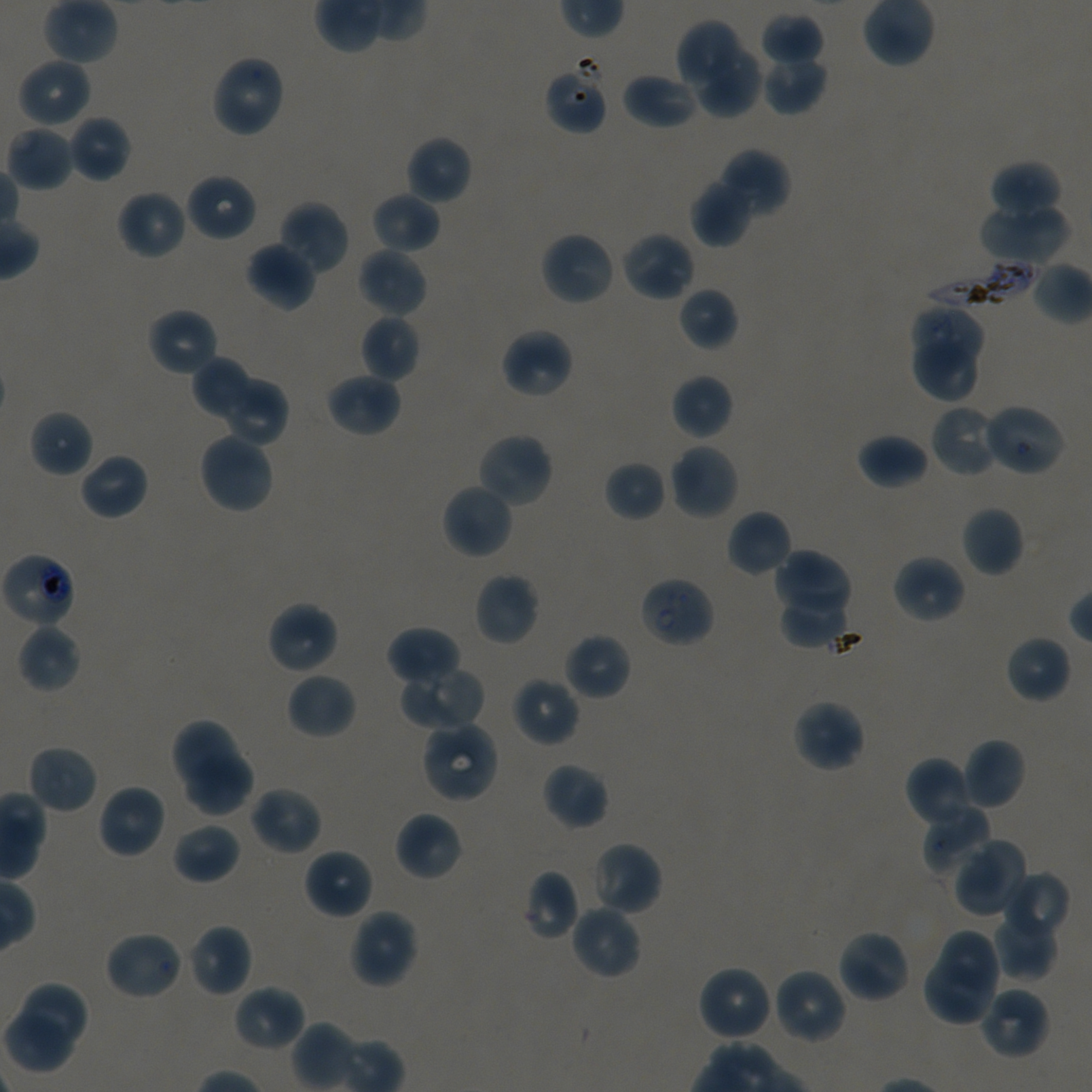

Approximate bounding rectangles given as corner coordinates in pixels from the top-left. Not every red blood cell is marked. A life-cycle stage — or a range of stages, where the recorded stages span more than one — follows each staged infected red blood cell.
Summary:
  - Locations of red blood cells of indeterminate infection status: (x1=545, y1=63, x2=608, y2=135)
  - Locations of infected red blood cells: (x1=924, y1=259, x2=1039, y2=310); (x1=0, y1=551, x2=76, y2=630) trophozoite; (x1=638, y1=575, x2=716, y2=649) early ring
  - Locations of uninfected red blood cells: (x1=760, y1=13, x2=824, y2=67), (x1=676, y1=20, x2=739, y2=87), (x1=696, y1=47, x2=763, y2=118), (x1=760, y1=53, x2=828, y2=115), (x1=210, y1=54, x2=286, y2=139), (x1=17, y1=57, x2=92, y2=128), (x1=621, y1=71, x2=699, y2=130), (x1=68, y1=115, x2=132, y2=183), (x1=5, y1=124, x2=75, y2=192), (x1=404, y1=135, x2=472, y2=206), (x1=716, y1=149, x2=790, y2=216), (x1=989, y1=160, x2=1061, y2=220), (x1=185, y1=172, x2=257, y2=242), (x1=690, y1=177, x2=754, y2=247), (x1=116, y1=189, x2=187, y2=260), (x1=371, y1=192, x2=441, y2=255), (x1=278, y1=200, x2=350, y2=275), (x1=979, y1=203, x2=1071, y2=265), (x1=539, y1=230, x2=617, y2=306), (x1=620, y1=230, x2=695, y2=302), (x1=245, y1=241, x2=316, y2=311), (x1=356, y1=247, x2=428, y2=318), (x1=1033, y1=261, x2=1092, y2=325), (x1=678, y1=286, x2=739, y2=351), (x1=908, y1=305, x2=983, y2=363), (x1=147, y1=307, x2=219, y2=378), (x1=359, y1=314, x2=420, y2=382), (x1=500, y1=327, x2=575, y2=399), (x1=912, y1=340, x2=977, y2=401), (x1=192, y1=357, x2=249, y2=418), (x1=325, y1=371, x2=402, y2=437), (x1=219, y1=374, x2=289, y2=448), (x1=670, y1=374, x2=733, y2=441), (x1=929, y1=404, x2=1002, y2=479), (x1=980, y1=404, x2=1065, y2=476), (x1=29, y1=410, x2=94, y2=477), (x1=198, y1=431, x2=275, y2=515), (x1=475, y1=431, x2=555, y2=509), (x1=857, y1=433, x2=929, y2=490), (x1=668, y1=442, x2=740, y2=521), (x1=79, y1=452, x2=149, y2=521), (x1=604, y1=460, x2=666, y2=522), (x1=441, y1=482, x2=514, y2=560), (x1=961, y1=505, x2=1025, y2=577), (x1=726, y1=509, x2=793, y2=577), (x1=774, y1=549, x2=852, y2=612), (x1=892, y1=554, x2=966, y2=624), (x1=473, y1=572, x2=541, y2=646), (x1=777, y1=596, x2=845, y2=650), (x1=266, y1=601, x2=340, y2=675), (x1=17, y1=623, x2=81, y2=693), (x1=386, y1=625, x2=461, y2=688), (x1=563, y1=632, x2=632, y2=701), (x1=1004, y1=634, x2=1072, y2=704), (x1=401, y1=665, x2=486, y2=731), (x1=286, y1=672, x2=357, y2=740), (x1=511, y1=676, x2=581, y2=748), (x1=791, y1=699, x2=866, y2=773), (x1=170, y1=718, x2=240, y2=794), (x1=420, y1=719, x2=500, y2=804), (x1=960, y1=738, x2=1027, y2=810), (x1=27, y1=744, x2=98, y2=815), (x1=183, y1=751, x2=252, y2=816), (x1=905, y1=756, x2=978, y2=830), (x1=542, y1=762, x2=609, y2=830), (x1=97, y1=784, x2=166, y2=860), (x1=249, y1=786, x2=323, y2=856), (x1=921, y1=803, x2=991, y2=877), (x1=394, y1=811, x2=463, y2=882), (x1=172, y1=822, x2=241, y2=884), (x1=953, y1=838, x2=1030, y2=917), (x1=590, y1=841, x2=663, y2=916), (x1=303, y1=848, x2=375, y2=920), (x1=522, y1=869, x2=581, y2=940), (x1=1002, y1=872, x2=1070, y2=944), (x1=569, y1=904, x2=642, y2=981), (x1=348, y1=908, x2=419, y2=988), (x1=992, y1=910, x2=1057, y2=981), (x1=186, y1=924, x2=253, y2=998), (x1=938, y1=928, x2=1002, y2=996), (x1=836, y1=929, x2=912, y2=1004), (x1=103, y1=930, x2=185, y2=1001), (x1=924, y1=958, x2=996, y2=1026), (x1=696, y1=964, x2=774, y2=1042), (x1=772, y1=967, x2=848, y2=1045), (x1=15, y1=981, x2=90, y2=1053), (x1=233, y1=983, x2=306, y2=1052), (x1=979, y1=985, x2=1051, y2=1060), (x1=0, y1=1008, x2=77, y2=1076)
  - Life-cycle stages observed: ring, trophozoite
  - Objective: 100x, oil immersion, numerical aperture 1.45
  - Image size: 1092×1092 pixels
  - Culture: static in-vitro Plasmodium falciparum strain NF54
  - Stain: Giemsa
  - Field of view: one from this slide
  - Preparation: thin blood smear
  - Donor blood group: A+/O+